Give the extent of all Plasmodium falciparum-infected red blood cells.
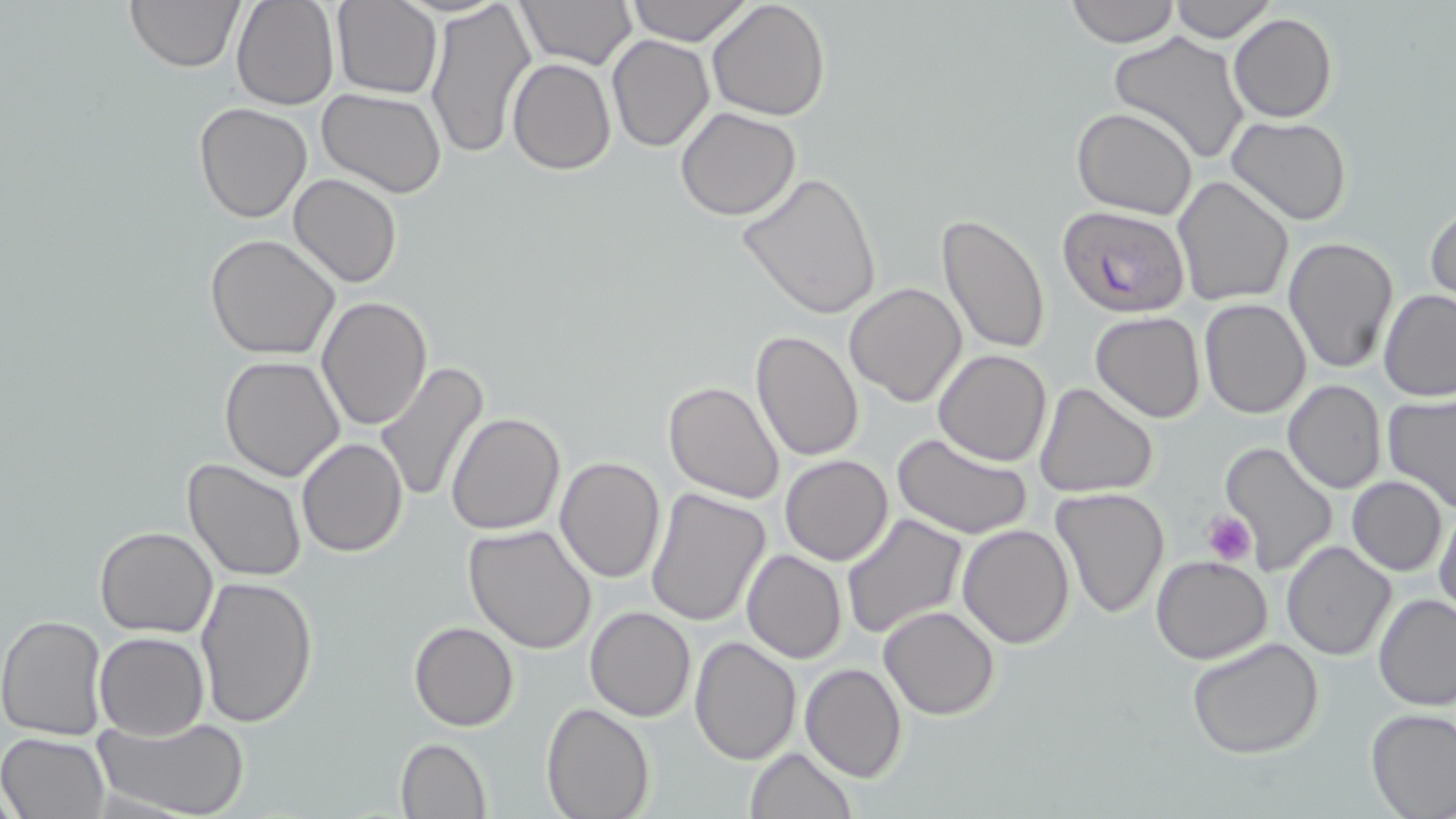

Approximate bounding boxes as [x1, y1, x2, y2] in pixels.
Plasmodium falciparum-infected red blood cells: [1057, 204, 1189, 316].

slide-level diagnosis = Plasmodium falciparum
stain = May-Grünwald-Giemsa
image size = 1456×819 pixels
uninfected red blood cell locations = approximate bounding boxes as [x1, y1, x2, y2] in pixels: [125, 0, 244, 72], [230, 0, 338, 110], [422, 0, 536, 161], [514, 0, 637, 71], [627, 0, 754, 45], [706, 0, 831, 121], [1065, 0, 1180, 46], [1170, 0, 1275, 42], [331, 1, 442, 99], [1228, 14, 1336, 122], [1107, 31, 1252, 165], [608, 34, 714, 152], [506, 58, 615, 174], [318, 89, 448, 199], [193, 101, 312, 222], [1071, 106, 1200, 220], [675, 107, 802, 221], [1226, 116, 1353, 225], [738, 170, 882, 319], [289, 173, 402, 287], [1171, 175, 1294, 307], [1426, 201, 1456, 306], [935, 214, 1052, 358], [205, 233, 340, 359], [1282, 237, 1400, 376], [843, 281, 967, 407], [1378, 289, 1456, 401], [315, 294, 432, 431], [1198, 299, 1312, 419], [1089, 312, 1207, 423], [750, 331, 864, 463], [932, 348, 1053, 465], [220, 355, 347, 481], [373, 362, 489, 505], [1283, 379, 1388, 494], [662, 380, 784, 503], [1036, 382, 1160, 498], [1382, 395, 1456, 516], [445, 412, 565, 535], [892, 431, 1031, 538], [297, 437, 408, 556], [1221, 441, 1339, 577], [780, 455, 893, 566], [554, 456, 666, 584], [183, 458, 307, 583], [1347, 476, 1447, 575], [646, 487, 772, 626], [1050, 488, 1169, 620], [1433, 502, 1456, 619], [840, 514, 967, 643], [464, 522, 598, 652], [956, 523, 1074, 648], [94, 526, 217, 638], [1282, 541, 1396, 660], [743, 549, 847, 663], [1150, 554, 1274, 664], [194, 575, 320, 730], [1372, 594, 1456, 710], [879, 604, 1000, 720], [585, 606, 696, 722], [0, 614, 109, 739], [409, 621, 519, 730], [95, 632, 207, 739], [1186, 635, 1325, 760], [689, 636, 801, 764], [799, 662, 907, 782], [540, 703, 654, 819], [1366, 707, 1456, 818], [94, 714, 250, 819], [0, 732, 109, 818], [393, 737, 491, 819], [743, 746, 856, 819]
platelet locations = approximate bounding boxes as [x1, y1, x2, y2] in pixels: [1201, 512, 1256, 566]
modality = optical microscopy
magnification = 1000x
preparation = thin blood smear
field of view = single